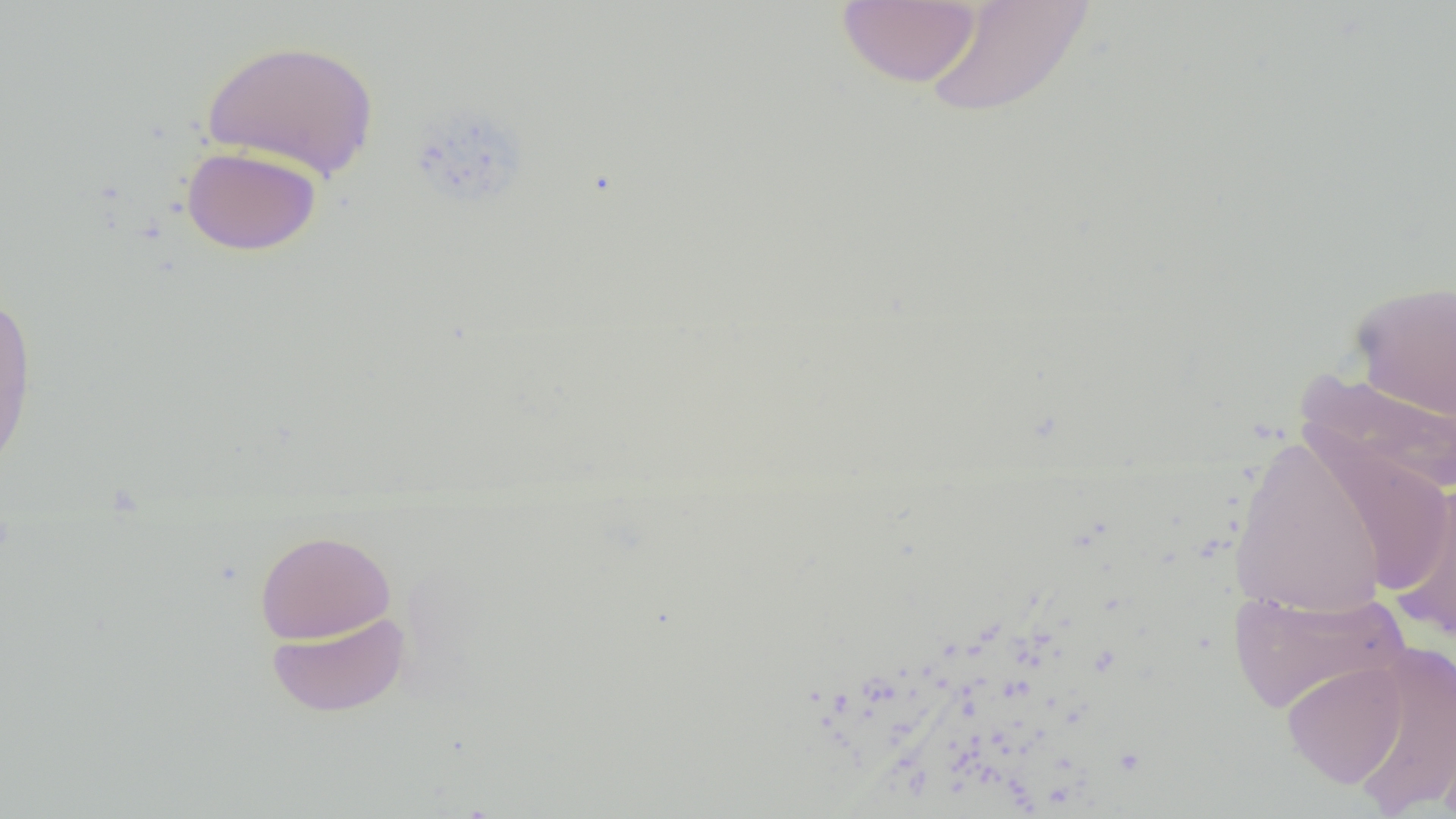
Approximate bounding boxes as (x1,y1)-(x2,y2) corner pairs in pixels. Uninfected red blood cell locations: (837,1)-(982,88), (922,1)-(1097,120), (200,38)-(380,180), (181,146)-(322,255), (1348,279)-(1456,422), (0,290)-(38,478), (1297,368)-(1456,499), (1303,432)-(1454,594), (1230,433)-(1388,619), (1391,481)-(1456,644), (255,529)-(396,644), (1228,586)-(1409,714), (267,611)-(410,717), (1347,644)-(1455,814), (1282,660)-(1407,788), (1436,702)-(1456,819). Slide-level diagnosis: negative for blood parasites. Image is 1456×819 pixels. Thin blood film. Optical microscopy. 1000x magnification. Single field of view.